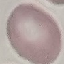
Malaria status: uninfected. Giemsa stain. Automatically extracted cell patch, resized to 64 × 64 pixels. Thin blood smear. Photographed with a smartphone camera at the microscope eyepiece.